Report the malaria status of this cell.
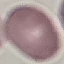
It is uninfected.

image type = automatically extracted cell patch, resized to 64 × 64 pixels
stain = Giemsa
capture = smartphone through the microscope eyepiece
preparation = thin blood film